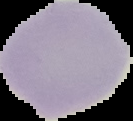

Summary:
  - Result: no Plasmodium parasites detected
  - Preparation: thin blood smear
  - Image size: 133×121 pixels
  - Image type: cell region segmented out of the field of view; surrounding area masked to black